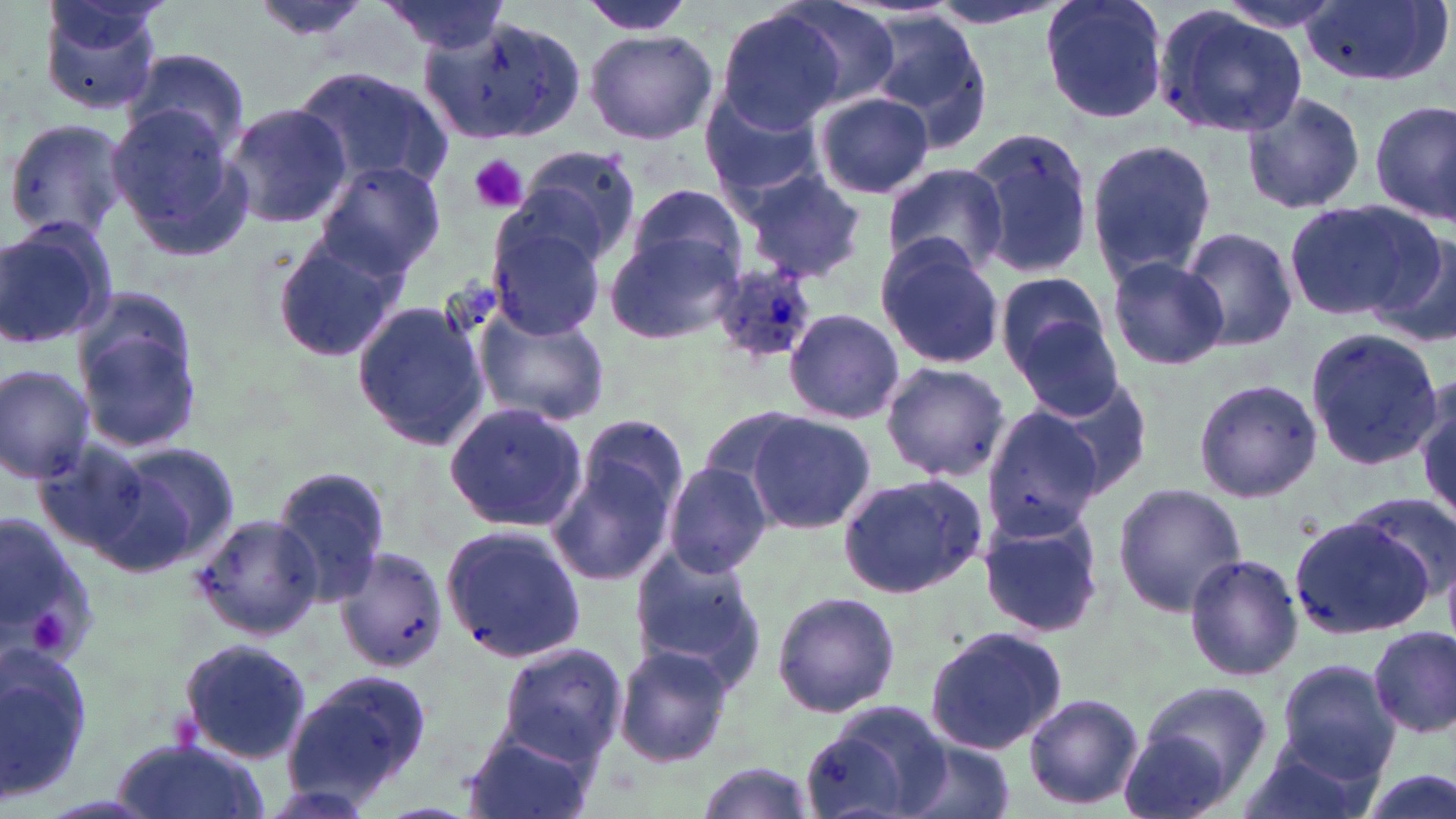

Summary:
  - Coordinate format: approximate bounding boxes as (x1, y1, x2, y2) in pixels
  - Platelet locations: (469, 155, 526, 213), (29, 611, 72, 652)
  - Uninfected red blood cell locations: (37, 0, 164, 117), (249, 0, 379, 50), (574, 0, 700, 37), (770, 0, 904, 112), (922, 0, 1067, 32), (1038, 0, 1169, 125), (1299, 0, 1449, 87), (376, 3, 513, 54), (1153, 5, 1310, 140), (711, 6, 849, 134), (417, 10, 588, 146), (864, 11, 995, 142), (583, 28, 718, 145), (123, 47, 252, 162), (291, 65, 453, 195), (1240, 90, 1368, 215), (814, 91, 935, 200), (698, 94, 827, 201), (1371, 99, 1455, 226), (220, 102, 351, 232), (107, 103, 253, 261), (3, 119, 132, 242), (963, 126, 1098, 279), (1084, 137, 1217, 288), (515, 146, 644, 265), (316, 159, 445, 279), (882, 161, 1010, 279), (741, 166, 868, 282), (622, 188, 750, 290), (1285, 198, 1437, 321), (486, 209, 611, 341), (0, 218, 117, 353), (1177, 226, 1300, 354), (1369, 227, 1456, 351), (604, 230, 744, 347), (267, 235, 405, 363), (874, 235, 1005, 370), (1106, 255, 1227, 371), (995, 271, 1111, 379), (70, 287, 205, 455), (351, 299, 489, 453), (470, 302, 614, 428), (783, 308, 904, 425), (1010, 320, 1128, 421), (1304, 328, 1443, 471), (879, 361, 1010, 483), (0, 362, 97, 484), (1194, 378, 1321, 503), (1021, 379, 1152, 501), (1414, 381, 1454, 522), (443, 402, 589, 532), (978, 405, 1113, 541), (744, 412, 877, 534), (552, 421, 689, 594), (31, 437, 179, 571), (102, 442, 242, 574), (662, 463, 771, 578), (270, 466, 394, 606), (836, 473, 988, 599), (1112, 482, 1247, 616), (1347, 491, 1456, 605), (0, 510, 98, 678), (977, 510, 1106, 639), (1291, 511, 1443, 639), (189, 512, 323, 642), (440, 523, 588, 664), (629, 544, 768, 683), (334, 545, 448, 677), (1183, 553, 1303, 682), (772, 590, 901, 718), (923, 626, 1066, 756), (1367, 626, 1455, 737), (178, 637, 313, 763), (1, 643, 98, 803), (495, 644, 628, 767), (614, 644, 736, 769), (1276, 660, 1398, 779), (286, 670, 435, 800), (1128, 681, 1272, 806), (1023, 692, 1143, 810), (803, 699, 950, 819), (1115, 724, 1240, 819), (460, 727, 599, 819), (110, 739, 268, 819), (899, 742, 1015, 819), (1230, 742, 1378, 819), (692, 762, 815, 818), (1349, 763, 1454, 819)
  - Plasmodium ovale-infected red blood cell locations: (705, 264, 818, 363)
  - Slide-level diagnosis: Plasmodium ovale
  - Image size: 1456×819 pixels
  - Field of view: one of a larger specimen
  - Preparation: thin blood film
  - Stain: May-Grünwald-Giemsa
  - Modality: light microscopy
  - Magnification: 1000x